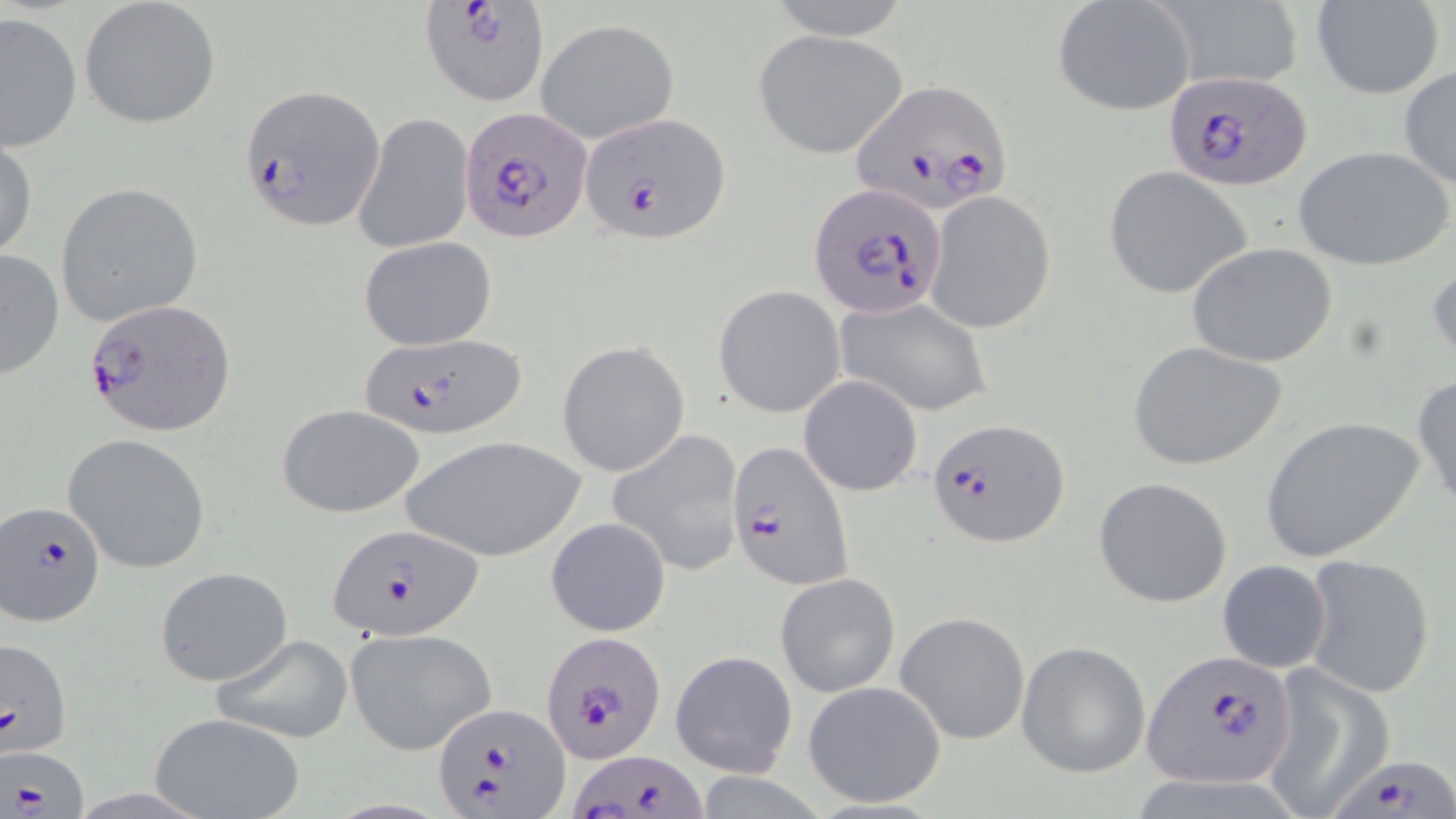

slide-level diagnosis = Plasmodium falciparum
magnification = 1000x
stain = May-Grünwald-Giemsa
field of view = single
uninfected red blood cell locations = approximate bounding boxes as [x1, y1, x2, y2] in pixels: [79, 0, 222, 130], [759, 0, 915, 40], [1052, 0, 1196, 118], [1312, 0, 1443, 99], [1151, 1, 1303, 93], [1, 11, 81, 153], [536, 19, 679, 144], [753, 30, 909, 160], [1398, 66, 1456, 191], [353, 112, 472, 256], [1, 135, 38, 261], [1292, 146, 1452, 271], [1103, 167, 1253, 299], [55, 181, 204, 327], [924, 191, 1056, 335], [358, 237, 496, 350], [1186, 241, 1339, 368], [0, 247, 65, 383], [1427, 253, 1456, 370], [714, 286, 845, 418], [835, 297, 994, 417], [1127, 339, 1289, 471], [556, 341, 690, 478], [1411, 372, 1456, 512], [798, 374, 923, 496], [277, 404, 425, 519], [1258, 417, 1425, 562], [606, 428, 747, 579], [63, 433, 211, 574], [398, 435, 585, 559], [1093, 476, 1234, 609], [546, 516, 672, 636], [1301, 553, 1437, 699], [1216, 559, 1332, 674], [155, 566, 293, 687], [776, 573, 899, 697], [895, 611, 1030, 745], [346, 628, 497, 756], [207, 633, 354, 744], [1015, 641, 1150, 778], [671, 650, 796, 778], [1262, 668, 1394, 816], [803, 680, 947, 810], [150, 710, 305, 819]
modality = light microscopy
image size = 1456×819 pixels
preparation = thin blood smear
Plasmodium falciparum-infected red blood cell locations = approximate bounding boxes as [x1, y1, x2, y2] in pixels: [417, 1, 550, 107], [1165, 69, 1312, 191], [853, 80, 1015, 215], [239, 85, 384, 231], [577, 110, 730, 244], [458, 111, 591, 243], [807, 184, 945, 321], [82, 298, 237, 439], [357, 331, 526, 440], [929, 417, 1071, 546], [725, 440, 855, 592], [0, 498, 107, 627], [327, 521, 483, 642], [535, 632, 667, 764], [0, 635, 71, 758], [1144, 652, 1297, 790], [432, 701, 570, 819], [2, 744, 90, 816], [573, 750, 708, 818], [1328, 752, 1455, 819]